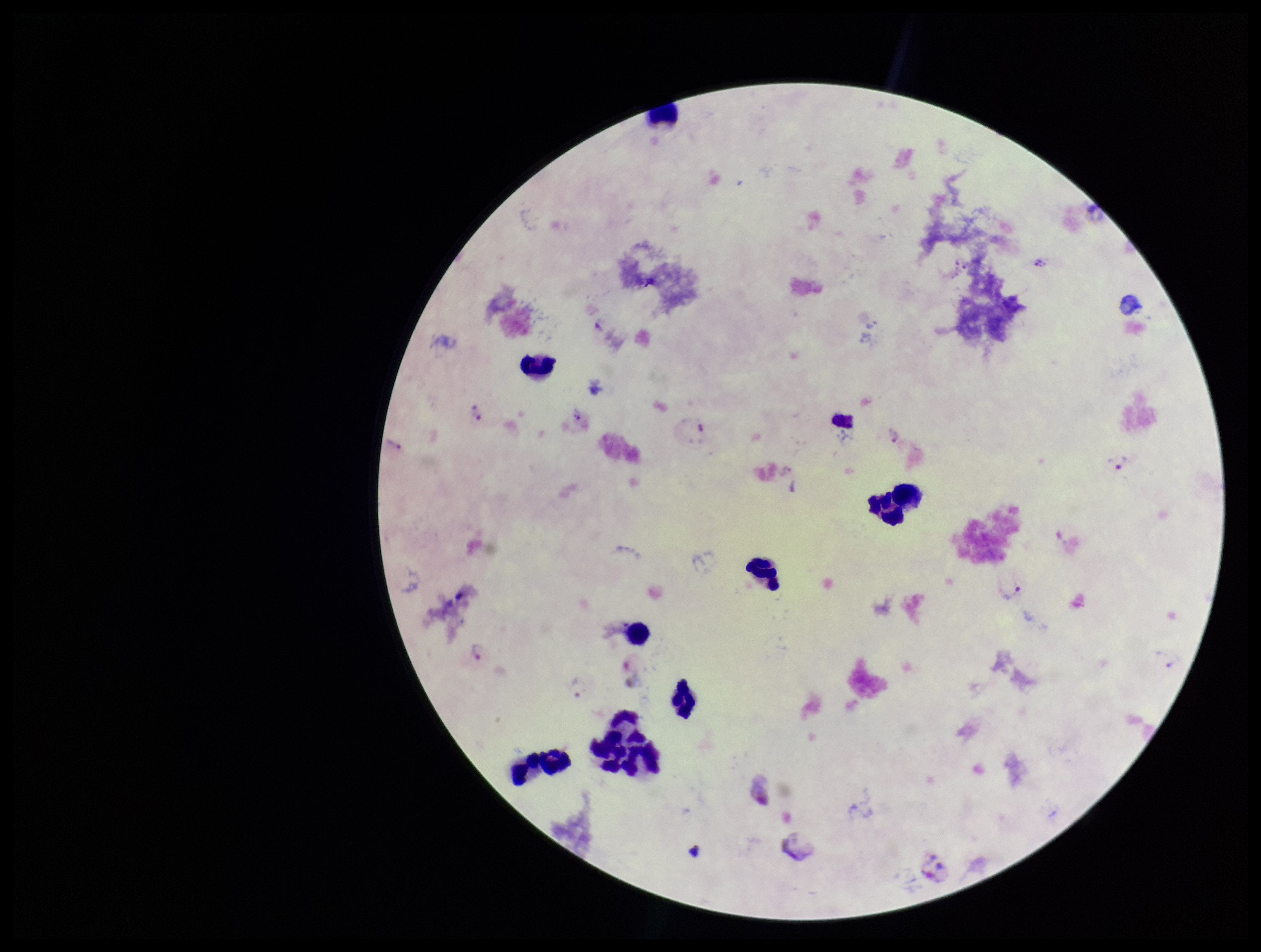
{
  "preparation": "thick blood smear",
  "capture": "smartphone photograph through the microscope eyepiece",
  "leukocyte_count": 9,
  "field_of_view": "one from this slide",
  "plasmodium_parasites": "detected",
  "stain": "Giemsa",
  "patient_malaria_status": "infected",
  "species_reported_for_this_patient": "Plasmodium vivax",
  "parasite_count": 7,
  "image_size": "1261×952 pixels"
}